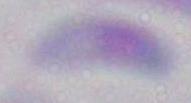

Summary:
  - Identification: Toxoplasma gondii
  - Modality: photomicrograph
  - Magnification: 1000x